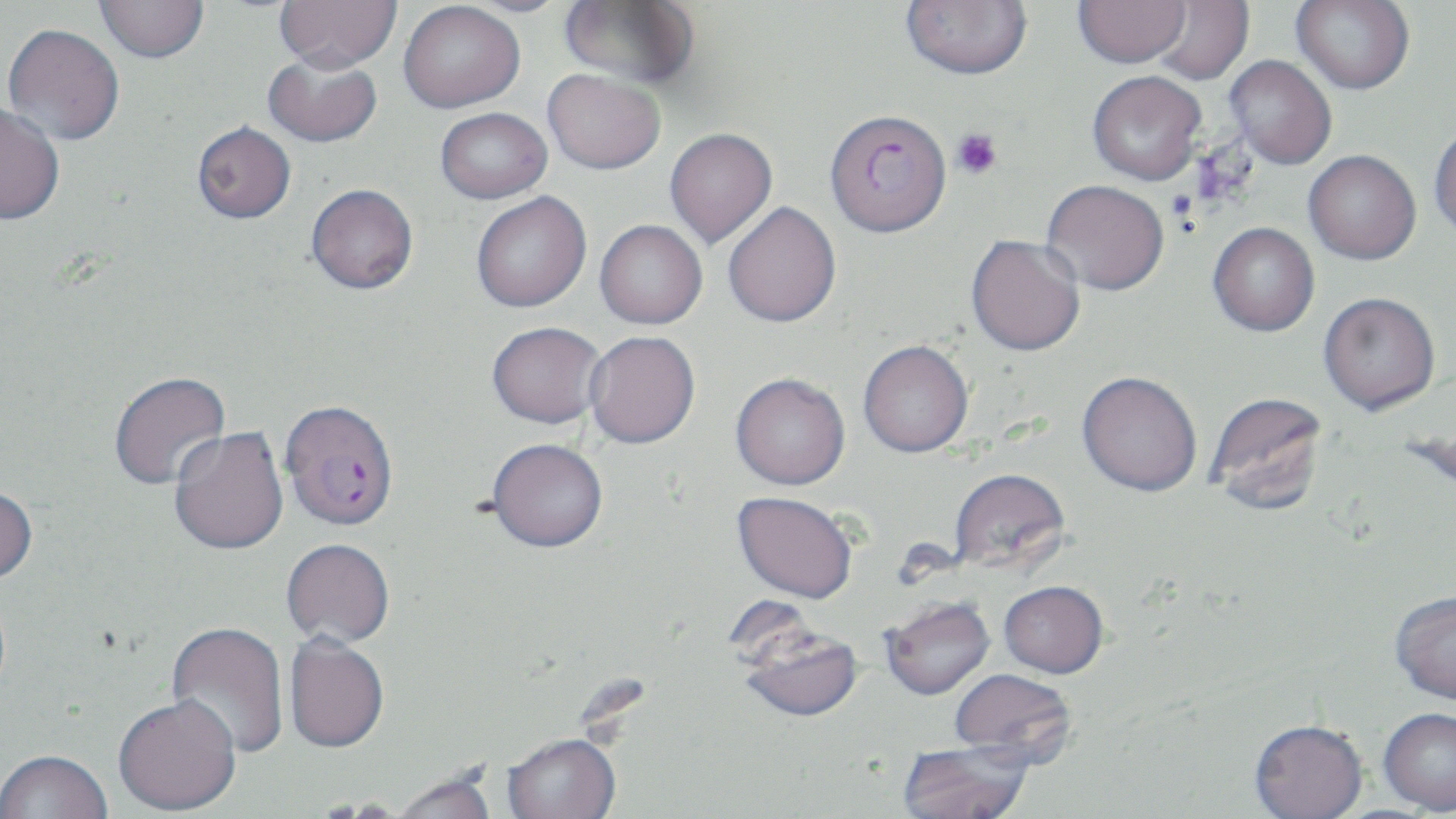 Approximate bounding boxes as (x1, y1, x2, y2) in pixels. Uninfected red blood cell locations: (94, 0, 209, 64), (274, 0, 401, 72), (901, 0, 1033, 80), (1073, 0, 1191, 68), (1291, 0, 1415, 94), (455, 1, 578, 17), (559, 1, 700, 90), (1148, 1, 1254, 85), (398, 2, 525, 113), (2, 23, 125, 146), (263, 53, 382, 147), (1225, 55, 1337, 169), (543, 69, 665, 174), (1087, 70, 1206, 184), (0, 101, 66, 225), (435, 107, 552, 204), (192, 121, 296, 224), (1429, 122, 1456, 240), (664, 127, 777, 248), (1303, 150, 1421, 265), (1041, 180, 1169, 296), (306, 184, 418, 294), (471, 192, 591, 313), (723, 201, 842, 327), (594, 219, 707, 329), (1208, 223, 1319, 337), (965, 233, 1086, 358), (1318, 291, 1440, 415), (487, 321, 607, 429), (584, 331, 701, 450), (858, 341, 973, 459), (109, 371, 231, 491), (1076, 373, 1202, 499), (730, 374, 851, 493), (1205, 391, 1329, 517), (168, 426, 289, 556), (485, 440, 609, 556), (949, 470, 1071, 577), (0, 486, 38, 587), (731, 494, 858, 607), (281, 540, 395, 649), (998, 584, 1108, 681), (1389, 592, 1456, 707), (880, 600, 997, 703), (165, 622, 290, 759), (736, 625, 864, 726), (283, 636, 389, 756), (949, 670, 1077, 770), (113, 697, 241, 817), (1378, 709, 1456, 816), (1248, 722, 1369, 819), (502, 735, 621, 819), (897, 742, 1032, 819), (0, 752, 113, 819), (388, 774, 500, 819). Plasmodium falciparum-infected red blood cell locations: (823, 108, 951, 238), (279, 400, 399, 533). Platelet locations: (950, 127, 1002, 179). Slide-level diagnosis: Plasmodium falciparum. One field of a larger specimen. May-Grünwald-Giemsa stain. Image is 1456×819 pixels. Thin blood smear. Captured at 1000x magnification. Light microscopy.